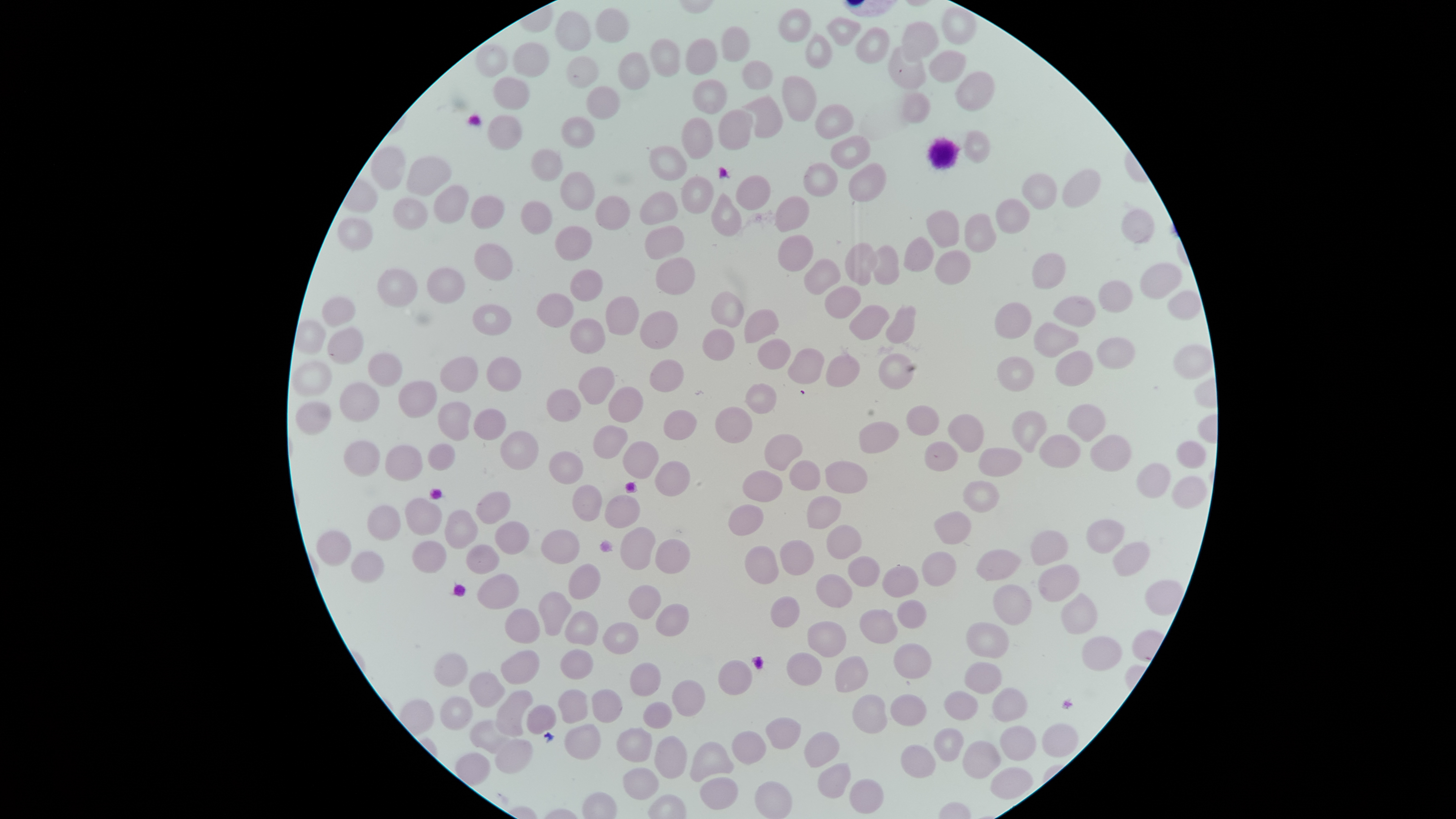 Approximate bounding boxes as [left, top, right, bottom] in pixels. Uninfected red blood cells: [942, 6, 976, 44], [779, 7, 811, 42], [596, 8, 628, 43], [556, 10, 590, 51], [827, 17, 862, 47], [903, 22, 939, 60], [721, 25, 749, 62], [856, 26, 889, 65], [806, 35, 833, 68], [650, 38, 681, 78], [685, 38, 718, 76], [512, 43, 550, 78], [477, 44, 508, 78], [889, 46, 926, 89], [928, 50, 967, 83], [618, 52, 649, 89], [565, 56, 600, 86], [743, 60, 774, 90], [955, 71, 994, 111], [782, 75, 818, 122], [494, 76, 530, 110], [692, 78, 728, 116], [587, 87, 621, 118], [904, 93, 931, 124], [740, 95, 783, 139], [815, 104, 855, 139], [718, 108, 752, 150], [488, 114, 523, 150], [562, 116, 593, 147], [683, 117, 713, 161], [964, 130, 991, 163], [830, 136, 871, 171], [650, 145, 688, 181], [371, 147, 405, 191], [531, 148, 561, 181], [405, 156, 451, 196], [848, 162, 886, 202], [803, 163, 838, 198], [1063, 168, 1102, 208], [559, 171, 595, 212], [1021, 173, 1057, 211], [736, 175, 773, 212], [681, 176, 715, 213], [435, 185, 468, 225], [640, 191, 678, 226], [711, 193, 741, 236], [472, 195, 503, 228], [595, 195, 629, 231], [775, 196, 809, 233], [394, 198, 430, 230], [996, 199, 1031, 233], [518, 201, 552, 234], [926, 209, 958, 250], [1121, 210, 1154, 245], [964, 212, 998, 252], [337, 217, 374, 251], [645, 225, 686, 259], [555, 226, 592, 260], [779, 234, 813, 272], [903, 236, 934, 271], [845, 242, 878, 285], [475, 243, 514, 280], [874, 244, 899, 285], [935, 250, 971, 285], [1033, 252, 1065, 290], [805, 257, 841, 294], [656, 259, 697, 297], [1140, 262, 1183, 300], [376, 267, 418, 307], [426, 268, 465, 303], [569, 268, 603, 302], [1098, 280, 1133, 313], [825, 286, 860, 319], [1167, 289, 1202, 322], [711, 291, 744, 327], [536, 294, 575, 328], [607, 296, 638, 335], [1053, 296, 1096, 327], [322, 297, 355, 327], [995, 302, 1030, 340], [472, 304, 512, 335], [850, 304, 889, 340], [885, 306, 915, 345], [744, 308, 780, 344], [640, 310, 678, 350], [570, 318, 607, 354], [1034, 322, 1079, 358], [328, 326, 364, 364], [703, 329, 736, 361], [1097, 337, 1136, 370], [758, 338, 790, 369], [1175, 344, 1213, 380], [789, 347, 824, 384], [1054, 351, 1093, 387], [367, 352, 402, 388], [825, 354, 859, 387], [879, 354, 915, 390], [439, 356, 478, 393], [487, 356, 521, 392], [997, 357, 1034, 393], [650, 359, 685, 393], [292, 360, 332, 398], [579, 367, 615, 406], [339, 381, 380, 424], [398, 381, 438, 419], [745, 383, 777, 415], [609, 387, 643, 423], [544, 388, 582, 424], [295, 402, 330, 436], [438, 402, 471, 440], [1067, 404, 1105, 443], [907, 405, 939, 436], [713, 406, 753, 444], [474, 408, 507, 440], [662, 409, 697, 440], [1012, 409, 1048, 454], [948, 412, 984, 454], [859, 421, 898, 455], [593, 425, 629, 459], [500, 430, 540, 471], [764, 433, 802, 471], [1039, 435, 1081, 468], [1089, 435, 1132, 471], [344, 440, 381, 478], [1177, 440, 1207, 469], [622, 441, 659, 479], [925, 441, 958, 471], [428, 443, 455, 471], [384, 446, 423, 482], [978, 446, 1021, 476], [548, 451, 583, 485], [789, 460, 820, 490], [655, 461, 691, 497], [825, 461, 868, 493], [1135, 463, 1171, 499], [743, 470, 782, 501], [1173, 476, 1208, 509], [963, 480, 999, 513], [572, 484, 603, 521], [477, 492, 510, 524], [605, 494, 641, 529], [806, 494, 841, 529], [405, 497, 442, 535], [729, 504, 765, 536], [366, 506, 401, 542], [445, 509, 478, 549], [934, 511, 972, 544], [1087, 520, 1125, 554], [495, 521, 530, 554], [825, 524, 861, 560], [622, 527, 656, 569], [1030, 529, 1067, 566], [316, 530, 351, 567], [541, 530, 579, 565], [655, 539, 689, 575], [413, 540, 446, 573], [780, 540, 814, 574], [1114, 542, 1151, 577], [467, 544, 501, 574], [745, 545, 780, 585], [976, 549, 1021, 582], [351, 551, 385, 582], [921, 551, 956, 588], [848, 554, 881, 587], [569, 563, 601, 599], [1038, 564, 1081, 602], [882, 565, 920, 597], [476, 574, 519, 611], [816, 574, 854, 609], [1143, 578, 1185, 616], [630, 585, 662, 620], [994, 585, 1031, 626], [539, 592, 572, 636], [1062, 593, 1100, 635], [770, 596, 800, 627], [898, 600, 928, 629], [657, 603, 690, 638], [505, 609, 541, 644], [859, 609, 899, 644], [565, 611, 598, 646], [807, 621, 847, 659], [602, 622, 638, 656], [966, 622, 1009, 659], [1082, 636, 1124, 672], [893, 643, 932, 680], [560, 649, 593, 681], [501, 650, 540, 685], [434, 652, 468, 688], [787, 652, 822, 686], [834, 655, 868, 693], [718, 660, 752, 696], [965, 661, 1002, 694], [632, 663, 661, 696], [469, 672, 504, 707], [672, 679, 705, 716], [557, 688, 588, 723], [993, 688, 1027, 721], [592, 689, 622, 724], [496, 690, 533, 736], [945, 691, 977, 722], [891, 693, 926, 726], [853, 694, 889, 734], [440, 695, 473, 731], [643, 702, 673, 729], [527, 705, 557, 734], [766, 717, 802, 749], [470, 719, 510, 753], [1042, 723, 1079, 759], [565, 724, 601, 761], [1001, 725, 1038, 762], [933, 726, 965, 764], [617, 728, 654, 763], [732, 730, 767, 766], [804, 731, 841, 768], [655, 736, 688, 779], [494, 739, 532, 773], [963, 741, 1001, 781], [690, 742, 734, 780], [901, 744, 937, 780], [817, 763, 852, 798], [991, 766, 1034, 800], [622, 767, 659, 801], [701, 777, 739, 810], [850, 777, 884, 815], [754, 780, 791, 818]. White blood cells: [925, 137, 962, 169]. Presence: no malaria parasites identified. One field of view of the specimen. Giemsa-stained preparation. Circular visible region. Thin blood film. Photographed with a smartphone camera through the microscope eyepiece. Image is 1456×819 pixels.